Report the malaria status of this cell.
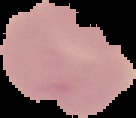

Uninfected.

Summary:
  - Preparation: thin blood smear
  - Image type: segmented cell region with the area outside set to black
  - Image size: 136×118 pixels